Classify this cell by malaria status.
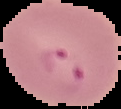

Parasitized.

{
  "preparation": "thin blood film",
  "image_type": "segmented cell region on a black background",
  "image_size": "121×109 pixels"
}